Report the malaria status of this cell.
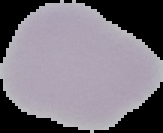

It is uninfected.

Image is 163×133 pixels. From a thin blood film. The area outside the segmented cell region is set to black.